Comment on the morphology of the erythrocytes.
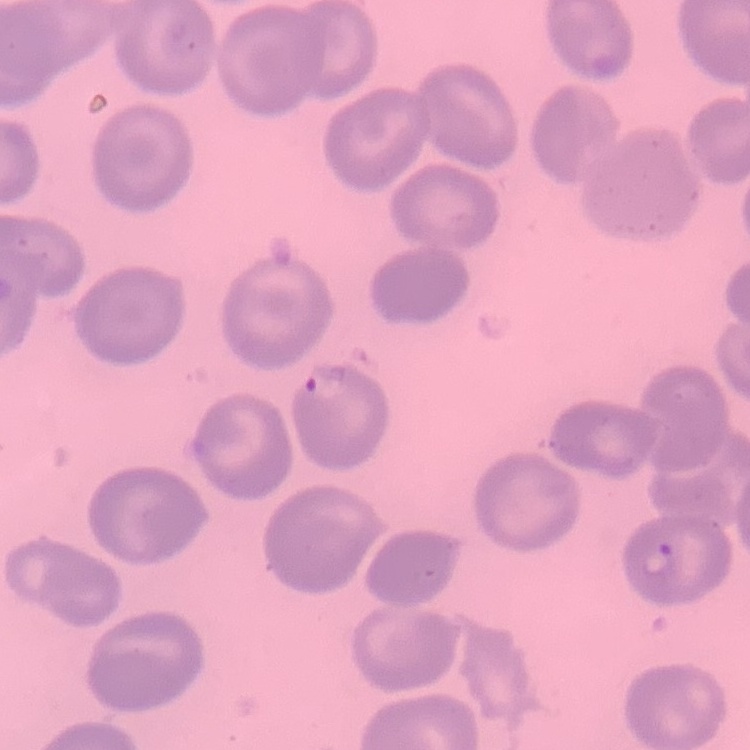
No rouleaux formation.

Thin blood smear. Square crop of a larger photomicrograph. Field's or Giemsa stain.